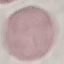

result = negative for malaria parasites
stain = Giemsa
image type = automatically extracted cell patch, resized to 64 × 64 pixels
preparation = thin blood film
capture = smartphone camera at the microscope eyepiece